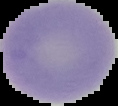
malaria status = uninfected
image size = 118×106 pixels
preparation = thin blood film
image type = segmented cell region with the area outside set to black